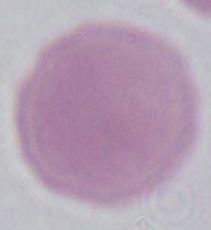
modality: micrograph
magnification: 1000x
identification: erythrocyte